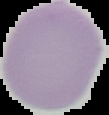

Summary:
  - Image type: segmented cell region on a black background
  - Image size: 109×115 pixels
  - Preparation: thin blood smear
  - Malaria status: uninfected